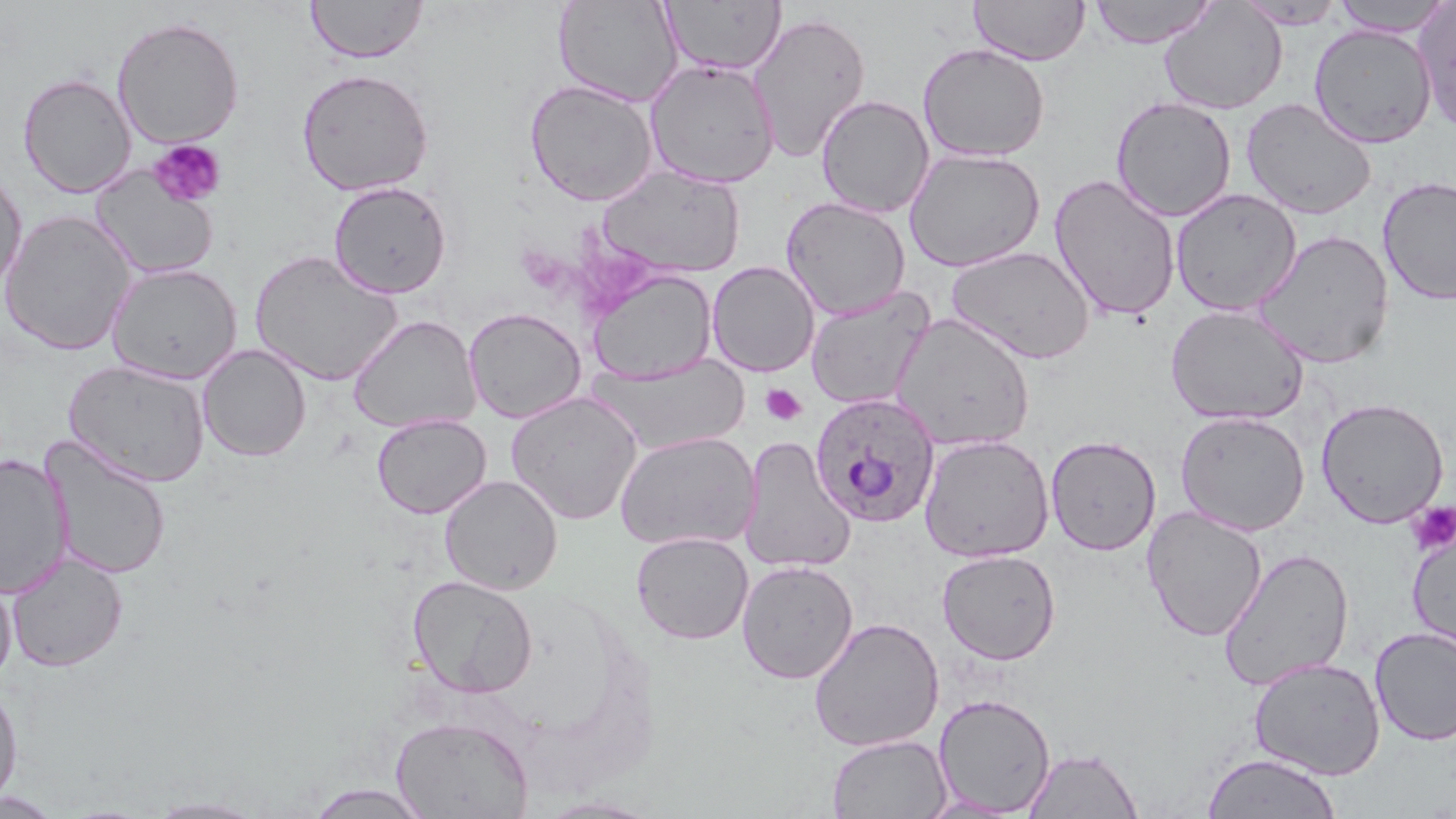
Summary:
  - Coordinate format: approximate bounding boxes as [x1, y1, x2, y2] in pixels
  - Uninfected red blood cell locations: [553, 0, 684, 108], [662, 0, 785, 75], [969, 0, 1090, 66], [1331, 0, 1452, 35], [306, 1, 429, 64], [1089, 1, 1217, 48], [1158, 1, 1287, 115], [1234, 1, 1349, 29], [1412, 1, 1456, 135], [747, 11, 871, 164], [112, 16, 245, 149], [1308, 23, 1438, 148], [917, 42, 1051, 162], [644, 58, 781, 188], [296, 68, 434, 196], [18, 72, 136, 198], [523, 79, 658, 207], [816, 95, 935, 217], [1110, 96, 1237, 222], [1240, 97, 1377, 220], [904, 148, 1046, 271], [596, 164, 746, 278], [89, 165, 219, 280], [0, 167, 27, 295], [1048, 173, 1182, 322], [1377, 176, 1456, 305], [328, 180, 452, 298], [1170, 188, 1302, 316], [781, 196, 911, 320], [0, 209, 137, 356], [1252, 229, 1395, 369], [946, 245, 1095, 365], [250, 250, 403, 386], [707, 261, 820, 376], [106, 262, 242, 384], [586, 268, 717, 384], [805, 287, 935, 410], [1165, 304, 1310, 426], [463, 307, 586, 424], [890, 313, 1036, 451], [348, 315, 480, 434], [197, 345, 312, 462], [588, 354, 750, 455], [63, 359, 210, 487], [506, 391, 643, 525], [1316, 397, 1449, 528], [1175, 410, 1311, 535], [371, 413, 491, 519], [614, 430, 759, 551], [918, 434, 1055, 562], [740, 435, 855, 573], [1046, 435, 1162, 556], [42, 439, 172, 580], [0, 452, 73, 599], [439, 474, 563, 595], [1142, 506, 1267, 642], [1407, 525, 1456, 654], [631, 531, 754, 645], [1217, 547, 1355, 691], [937, 549, 1061, 665], [6, 552, 129, 673], [736, 559, 858, 684], [0, 567, 16, 684], [407, 574, 539, 698], [808, 616, 945, 752], [1370, 625, 1456, 746], [1248, 657, 1386, 780], [0, 680, 23, 808], [933, 693, 1056, 816], [391, 717, 535, 818], [826, 734, 951, 818], [1022, 747, 1143, 818], [1201, 752, 1341, 818], [300, 782, 434, 819], [0, 792, 66, 818], [144, 796, 271, 818]
  - Plasmodium ovale-infected red blood cell locations: [810, 392, 941, 528]
  - Platelet locations: [148, 140, 226, 207], [760, 384, 807, 426], [1407, 501, 1456, 554]
  - Slide-level diagnosis: Plasmodium ovale
  - Preparation: thin blood film
  - Magnification: 1000x
  - Image size: 1456×819 pixels
  - Field of view: one of a larger specimen
  - Stain: May-Grünwald-Giemsa
  - Modality: optical microscopy